Assess this cell for malaria.
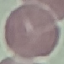
Uninfected.

Automatically extracted cell patch, resized to 64 × 64 pixels. Giemsa stain. Acquired by smartphone through the microscope eyepiece. Thin smear of blood.